Name the cell type shown.
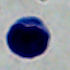

This is a leukocyte.

Summary:
  - Modality: photomicrograph
  - Magnification: 1000x